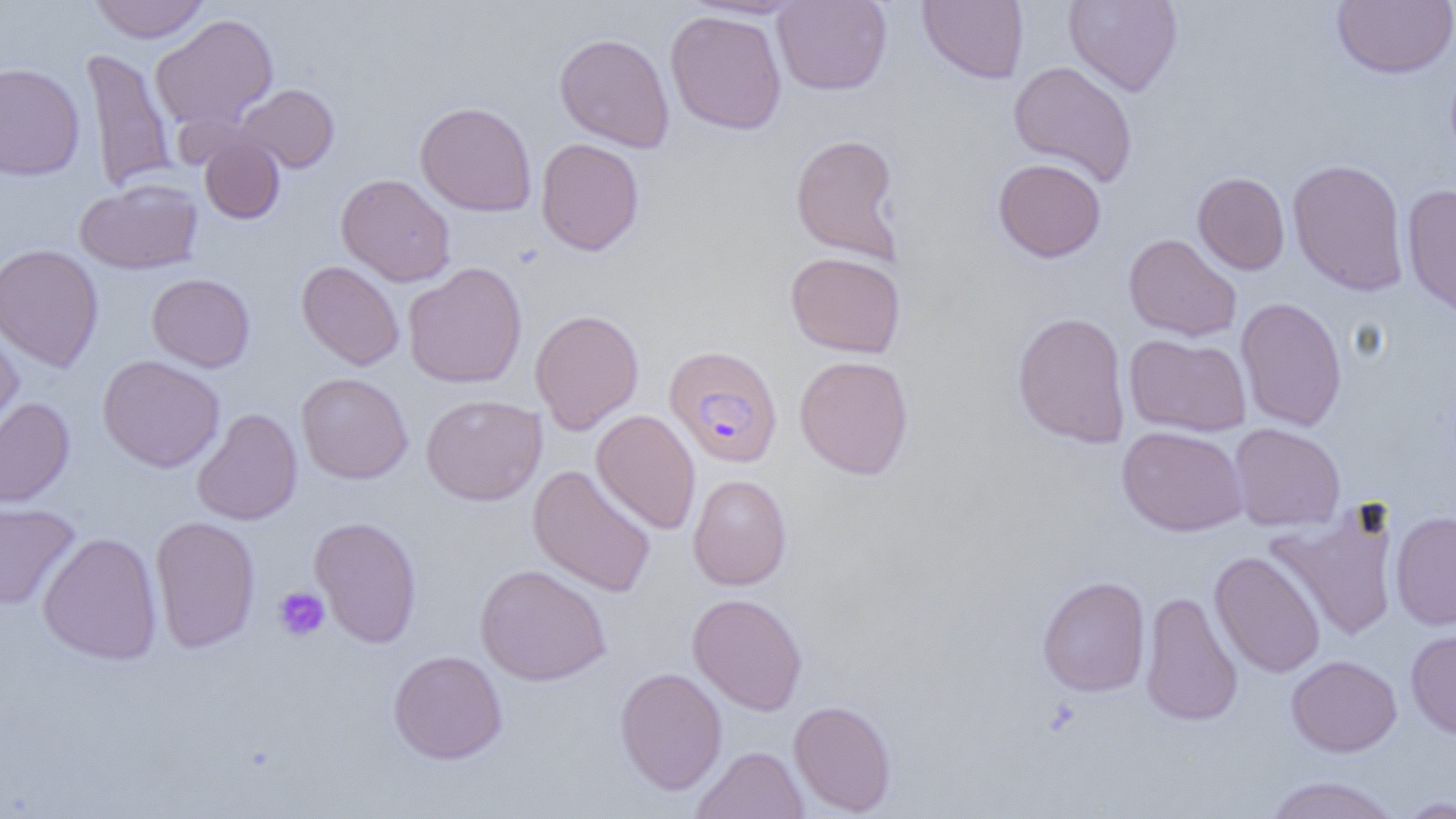
slide-level diagnosis = Plasmodium falciparum
magnification = 1000x
platelet locations = approximate bounding boxes as (x1, y1, x2, y2) in pixels: (273, 586, 330, 642)
uninfected red blood cell locations = approximate bounding boxes as (x1, y1, x2, y2) in pixels: (88, 0, 211, 43), (918, 0, 1029, 84), (1064, 0, 1183, 96), (1331, 0, 1456, 79), (773, 1, 892, 95), (665, 9, 787, 135), (150, 14, 279, 131), (554, 32, 675, 153), (81, 48, 177, 193), (1007, 60, 1138, 187), (0, 62, 85, 181), (235, 83, 339, 173), (415, 101, 537, 217), (789, 133, 904, 265), (199, 135, 285, 224), (535, 138, 645, 256), (992, 158, 1107, 262), (1287, 158, 1410, 296), (1192, 172, 1290, 274), (336, 173, 456, 287), (75, 179, 203, 275), (1401, 183, 1456, 320), (1123, 233, 1241, 341), (0, 243, 104, 373), (785, 251, 906, 358), (296, 260, 405, 371), (402, 262, 527, 388), (146, 273, 255, 372), (1235, 297, 1347, 431), (530, 308, 645, 435), (1012, 311, 1131, 448), (0, 320, 24, 445), (1124, 334, 1251, 437), (794, 354, 914, 480), (97, 355, 225, 473), (296, 372, 413, 484), (420, 393, 547, 506), (0, 398, 75, 508), (192, 408, 303, 526), (591, 409, 701, 535), (1229, 423, 1345, 532), (1116, 425, 1248, 536), (528, 464, 656, 598), (687, 474, 792, 590), (0, 499, 80, 609), (1266, 502, 1401, 642), (1390, 511, 1456, 630), (309, 515, 422, 648), (149, 516, 261, 653), (37, 532, 163, 665), (1209, 550, 1325, 678), (475, 563, 612, 686), (1037, 575, 1150, 697), (1140, 590, 1243, 727), (687, 592, 807, 715), (1406, 627, 1456, 739), (388, 650, 508, 764), (1286, 655, 1401, 756), (614, 666, 727, 796), (788, 699, 897, 816), (692, 746, 808, 819), (1262, 775, 1401, 819), (1394, 795, 1456, 818)
image size = 1456×819 pixels
field of view = one of a larger specimen
preparation = thin blood smear
modality = light microscopy
Plasmodium falciparum-infected red blood cell locations = approximate bounding boxes as (x1, y1, x2, y2) in pixels: (663, 344, 783, 468)